State the blood parasite species.
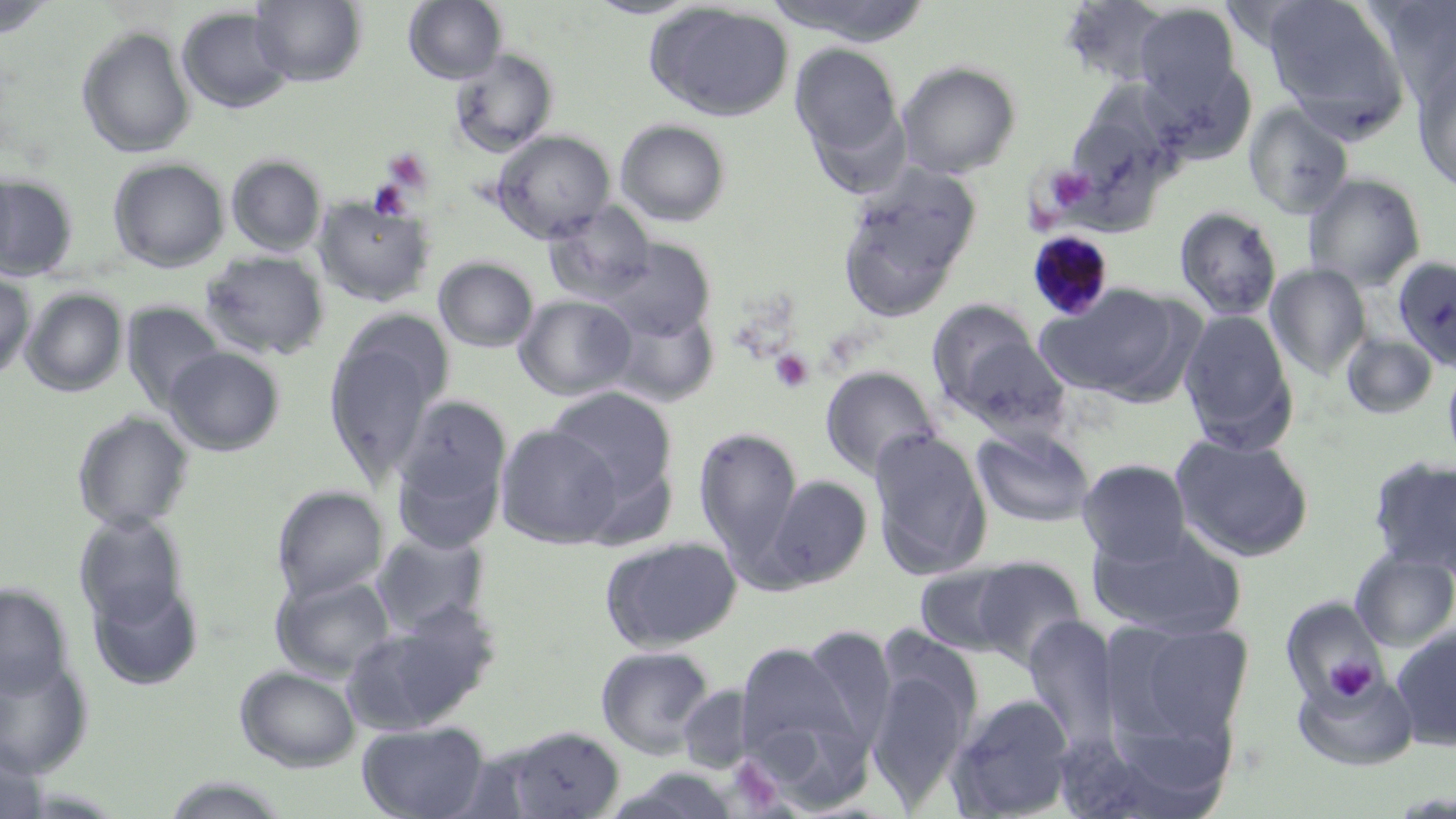

Plasmodium malariae.

{
  "uninfected_red_blood_cell_locations": "approximate bounding boxes as (x1, y1, x2, y2) in pixels: (250, 0, 367, 86), (403, 0, 507, 84), (582, 0, 706, 19), (767, 0, 932, 45), (1060, 0, 1174, 88), (1369, 0, 1456, 106), (0, 1, 57, 39), (1261, 1, 1412, 140), (645, 2, 796, 122), (1133, 3, 1242, 111), (176, 6, 293, 114), (76, 25, 196, 159), (790, 43, 907, 173), (448, 48, 558, 157), (1414, 59, 1456, 194), (898, 61, 1021, 178), (1067, 81, 1190, 193), (1243, 103, 1355, 218), (615, 119, 731, 227), (492, 130, 616, 242), (226, 155, 327, 256), (108, 157, 229, 272), (0, 162, 19, 272), (839, 167, 981, 315), (1304, 173, 1426, 290), (0, 175, 78, 281), (313, 196, 434, 306), (544, 201, 657, 302), (1175, 206, 1283, 320), (602, 240, 715, 341), (200, 249, 330, 361), (434, 256, 539, 352), (1394, 256, 1456, 373), (1265, 263, 1372, 378), (0, 271, 35, 382), (1039, 283, 1186, 400), (21, 288, 128, 397), (514, 294, 636, 400), (925, 298, 1048, 416), (121, 302, 226, 412), (607, 305, 718, 406), (1178, 309, 1298, 452), (324, 319, 452, 484), (1342, 332, 1438, 419), (163, 346, 285, 455), (1442, 357, 1456, 471), (820, 366, 940, 479), (545, 386, 678, 513), (390, 395, 512, 552), (72, 410, 194, 531), (495, 423, 623, 548), (694, 426, 802, 563), (972, 426, 1096, 527), (869, 428, 993, 579), (1171, 434, 1314, 561), (1369, 454, 1456, 578), (1078, 458, 1191, 565), (762, 474, 873, 588), (272, 486, 389, 602), (74, 511, 189, 628), (1090, 525, 1246, 638), (371, 528, 490, 635), (600, 536, 742, 652), (1350, 548, 1456, 650), (968, 556, 1087, 668), (914, 561, 1029, 658), (271, 573, 395, 680), (87, 577, 204, 691), (0, 583, 72, 696), (1280, 597, 1390, 709), (343, 608, 494, 733), (1023, 616, 1121, 749), (1106, 619, 1254, 753), (799, 626, 896, 750), (1392, 626, 1456, 752), (734, 641, 862, 781), (596, 645, 716, 759), (865, 654, 978, 807), (0, 655, 93, 778), (235, 665, 361, 771), (1292, 666, 1418, 770), (677, 684, 756, 771), (946, 694, 1077, 818), (357, 721, 489, 819), (500, 725, 626, 818), (0, 743, 49, 819), (159, 775, 294, 818)",
  "stain": "May-Grünwald-Giemsa",
  "modality": "light microscopy",
  "platelet_locations": "approximate bounding boxes as (x1, y1, x2, y2) in pixels: (382, 148, 433, 194), (1044, 166, 1095, 213), (368, 179, 413, 221), (769, 350, 814, 393), (1324, 658, 1375, 702)",
  "magnification": "1000x",
  "field_of_view": "single",
  "plasmodium_malariae_infected_red_blood_cell_locations": "approximate bounding boxes as (x1, y1, x2, y2) in pixels: (1027, 230, 1117, 321)",
  "preparation": "thin blood smear",
  "image_size": "1456×819 pixels"
}